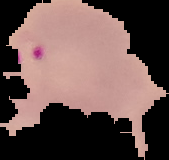
malaria status = parasitized
preparation = thin blood smear
image type = segmented cell region on a black background
image size = 169×160 pixels